Identify the parasite.
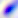
This is Toxoplasma gondii.

modality = micrograph
magnification = 400x